Name the cell type shown.
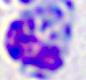
This is a leukocyte.

Captured at 400x magnification. Micrograph.